Assess this cell for malaria.
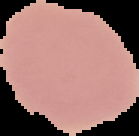

Uninfected.

Summary:
  - Preparation: thin blood smear
  - Image size: 139×136 pixels
  - Image type: segmented cell region on a black background